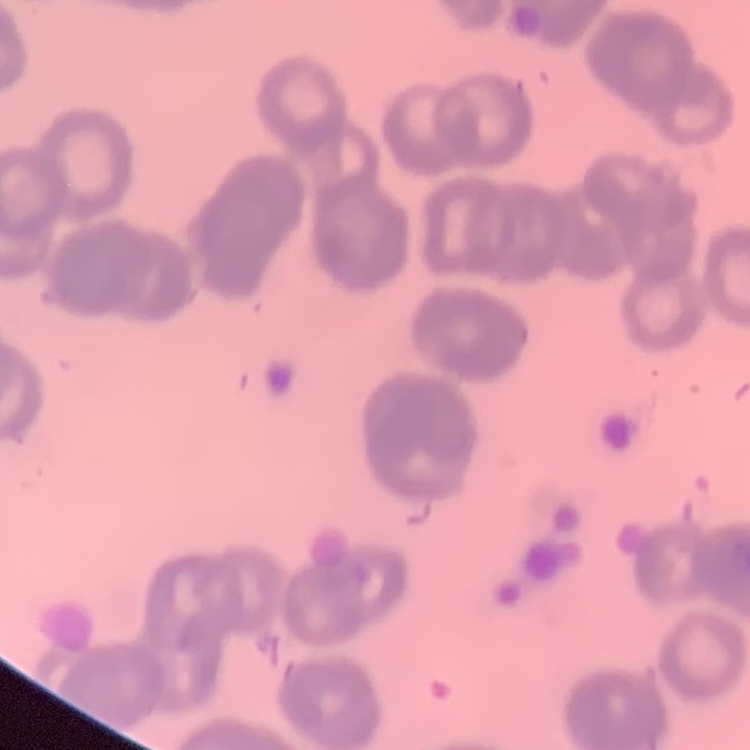
Summary:
  - Red blood cell morphology: rouleaux formation
  - Stain: Field's or Giemsa
  - Preparation: thin blood film
  - Image type: square crop of a larger photomicrograph